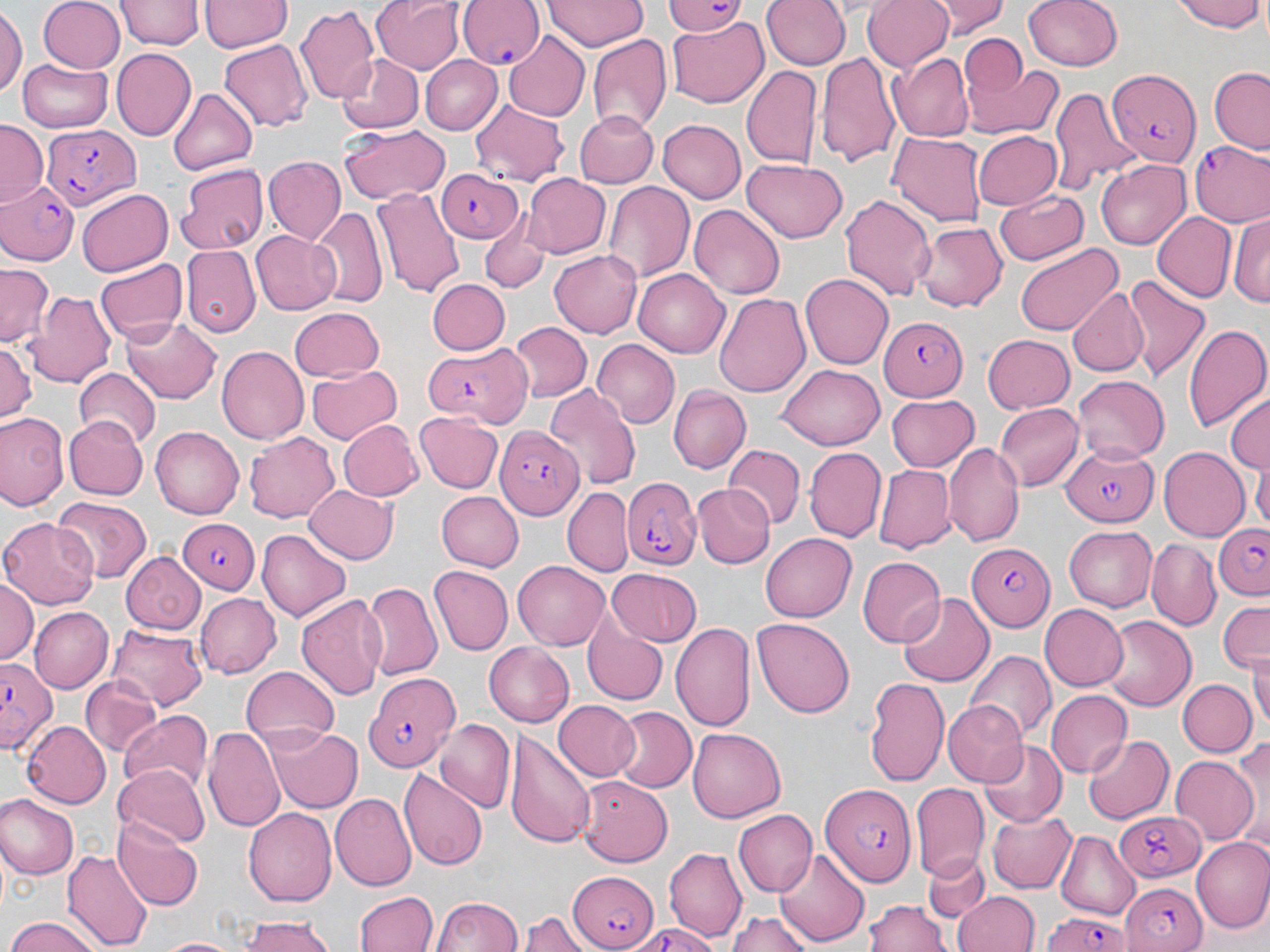

Approximate bounding boxes as (x1,y1)-(x2,y2) corner pairs in pixels. Plasmodium falciparum-infected red blood cell locations: (456,0)-(544,74), (664,0)-(748,38), (1105,66)-(1199,166), (42,126)-(138,210), (1189,141)-(1270,229), (435,166)-(522,245), (0,178)-(84,266), (881,316)-(969,400), (424,347)-(523,423), (497,427)-(584,519), (1060,443)-(1156,525), (619,473)-(702,569), (175,516)-(258,593), (1212,524)-(1269,602), (965,540)-(1052,628), (1,657)-(61,753), (361,672)-(459,773), (821,780)-(918,889), (1113,808)-(1207,882), (565,868)-(658,949), (1120,881)-(1209,951), (1039,909)-(1134,952). Uninfected red blood cell locations: (39,0)-(123,73), (198,0)-(290,53), (373,0)-(466,75), (544,0)-(647,51), (760,0)-(847,70), (863,0)-(954,72), (930,0)-(1009,37), (1023,0)-(1122,71), (1174,0)-(1266,33), (116,1)-(201,50), (296,5)-(381,108), (0,7)-(24,100), (667,19)-(770,108), (501,31)-(591,122), (957,31)-(1028,113), (586,33)-(672,134), (218,39)-(312,133), (109,46)-(195,138), (816,50)-(900,166), (893,53)-(975,142), (335,54)-(422,133), (965,56)-(1063,138), (422,57)-(501,135), (19,58)-(113,132), (740,63)-(821,172), (1207,67)-(1270,153), (1049,85)-(1138,196), (167,88)-(257,175), (471,99)-(567,183), (572,110)-(657,188), (659,119)-(746,203), (0,122)-(46,205), (340,123)-(450,205), (971,130)-(1062,210), (887,132)-(986,225), (265,156)-(345,242), (1096,159)-(1190,249), (741,160)-(848,244), (175,163)-(270,255), (523,173)-(611,259), (603,182)-(694,282), (373,188)-(463,300), (75,189)-(173,277), (994,190)-(1090,266), (839,192)-(938,303), (690,204)-(784,300), (311,208)-(388,307), (1153,211)-(1235,301), (1230,212)-(1270,306), (1187,215)-(1270,304), (915,222)-(1006,313), (252,229)-(343,315), (479,230)-(548,292), (1014,242)-(1124,335), (181,246)-(258,337), (549,249)-(641,338), (95,258)-(187,341), (0,262)-(56,345), (633,268)-(732,357), (801,274)-(894,369), (1122,275)-(1210,382), (427,278)-(510,356), (1066,286)-(1149,377), (26,288)-(118,391), (714,292)-(811,397), (288,305)-(385,380), (122,314)-(222,405), (507,321)-(591,403), (1184,323)-(1270,433), (981,333)-(1075,413), (0,339)-(36,427), (592,342)-(680,428), (215,344)-(309,446), (777,364)-(884,448), (306,365)-(400,446), (74,369)-(162,450), (1073,374)-(1171,460), (544,384)-(641,492), (668,385)-(749,472), (1225,392)-(1269,478), (886,393)-(980,471), (995,400)-(1083,489), (0,410)-(67,512), (415,410)-(504,494), (62,414)-(148,501), (341,421)-(419,500), (150,427)-(243,519), (245,432)-(340,522), (944,444)-(1024,547), (726,446)-(804,526), (804,446)-(886,543), (1158,448)-(1251,541), (1252,456)-(1270,535), (871,462)-(955,550), (695,484)-(770,568), (306,485)-(397,563), (562,485)-(633,577), (436,490)-(523,571), (53,495)-(151,580), (0,517)-(100,609), (1062,525)-(1158,612), (257,530)-(350,621), (761,530)-(859,622), (1145,538)-(1221,627), (122,551)-(205,634), (858,556)-(945,647), (513,561)-(611,649), (429,567)-(513,656), (608,569)-(702,646), (1,577)-(38,663), (362,582)-(444,684), (296,591)-(388,703), (899,592)-(993,687), (196,593)-(280,679), (1218,600)-(1268,673), (1040,604)-(1129,691), (29,605)-(112,690), (752,617)-(855,717), (1104,617)-(1194,713), (671,621)-(756,733), (584,622)-(668,705), (106,625)-(208,709), (484,642)-(574,727), (1249,643)-(1269,739), (965,651)-(1055,742), (881,665)-(969,852), (241,667)-(340,746), (80,675)-(162,757), (865,676)-(948,786), (1176,678)-(1255,757), (1045,688)-(1132,776), (551,700)-(641,781), (944,701)-(1026,784), (608,707)-(696,793), (119,712)-(212,798), (434,720)-(515,812), (22,722)-(112,806), (206,724)-(286,831), (269,726)-(362,812), (688,728)-(786,822), (508,731)-(595,850), (1083,734)-(1174,824), (1233,736)-(1269,849), (978,740)-(1065,827), (1169,754)-(1259,847), (115,764)-(210,847), (398,767)-(488,870), (577,775)-(672,866), (910,781)-(987,878), (330,794)-(415,889), (0,796)-(77,879), (244,807)-(337,905), (986,808)-(1076,895), (731,810)-(815,897), (113,814)-(204,910), (1054,832)-(1140,916), (1191,837)-(1270,935), (663,846)-(746,943), (63,847)-(152,951), (774,849)-(869,947), (921,853)-(989,926), (355,890)-(438,952), (954,892)-(1039,952), (433,896)-(524,952), (868,898)-(950,952), (724,908)-(815,952), (518,912)-(589,952), (237,913)-(340,952), (4,917)-(106,952), (155,935)-(246,952). Slide-level diagnosis: Plasmodium falciparum. 1000x magnification. Thin blood smear. Image is 1270×952 pixels. Single field of view. May-Grünwald-Giemsa stain. Light microscopy.